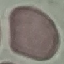

Summary:
  - Result: no malaria parasites detected
  - Image type: automatically extracted cell patch, resized to 64 × 64 pixels
  - Capture: smartphone through the microscope eyepiece
  - Stain: Giemsa
  - Preparation: thin smear